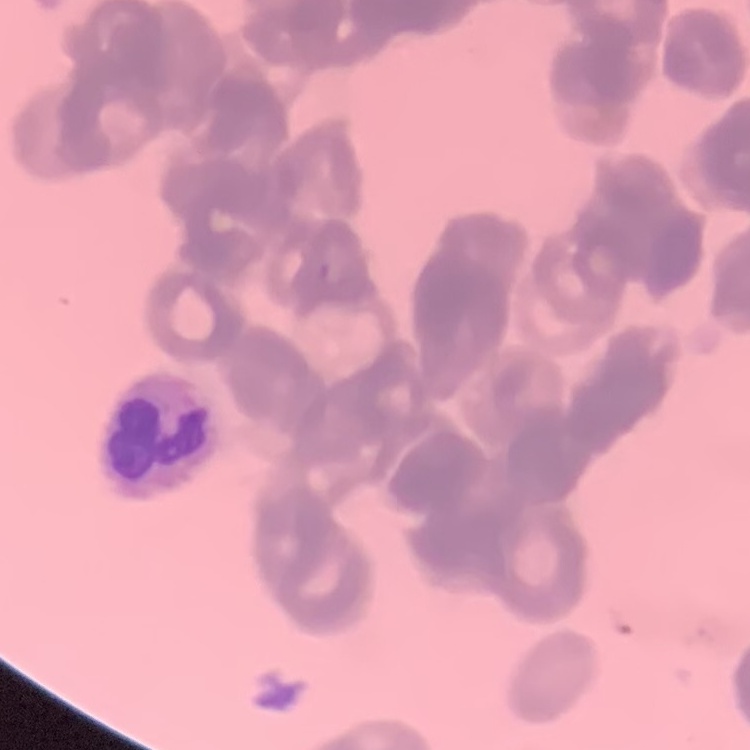
{
  "red_blood_cell_morphology": "rouleaux formation",
  "stain": "Field's or Giemsa",
  "preparation": "thin blood smear",
  "image_type": "square crop of a larger photomicrograph"
}